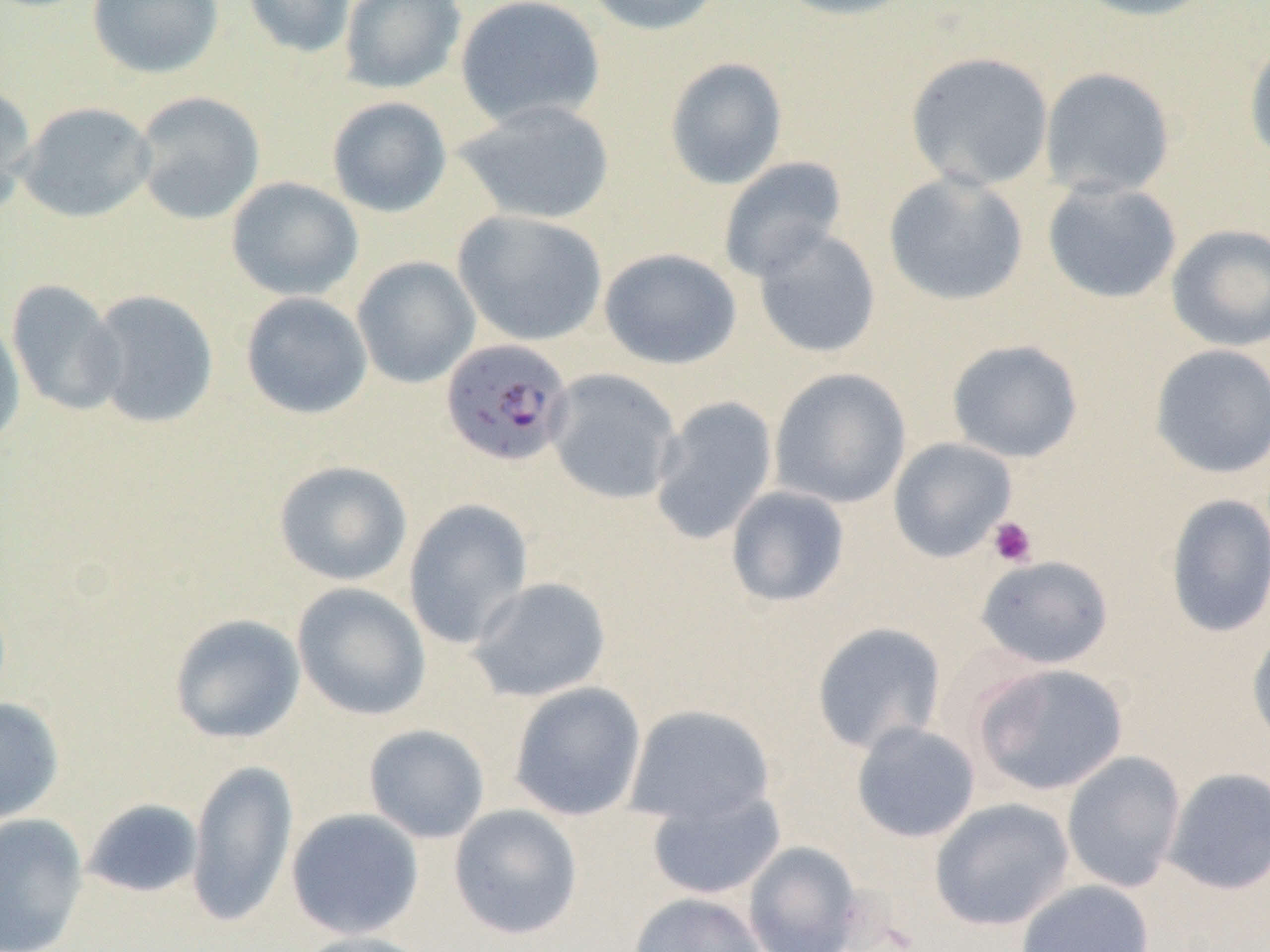

Summary:
  - Coordinate format: approximate bounding boxes as named x1/y1/x2/y2 corners in pixels
  - Uninfected red blood cell locations: (x1=86, y1=0, x2=224, y2=79), (x1=243, y1=0, x2=357, y2=59), (x1=338, y1=0, x2=467, y2=94), (x1=454, y1=0, x2=605, y2=129), (x1=582, y1=0, x2=729, y2=36), (x1=771, y1=0, x2=920, y2=21), (x1=1070, y1=0, x2=1220, y2=22), (x1=1244, y1=35, x2=1270, y2=167), (x1=904, y1=51, x2=1055, y2=192), (x1=664, y1=57, x2=788, y2=190), (x1=1039, y1=67, x2=1176, y2=199), (x1=0, y1=81, x2=37, y2=216), (x1=132, y1=91, x2=266, y2=225), (x1=327, y1=96, x2=452, y2=217), (x1=453, y1=99, x2=616, y2=225), (x1=17, y1=102, x2=156, y2=223), (x1=718, y1=157, x2=848, y2=283), (x1=883, y1=171, x2=1029, y2=306), (x1=225, y1=176, x2=363, y2=302), (x1=1042, y1=179, x2=1182, y2=304), (x1=452, y1=210, x2=607, y2=346), (x1=1165, y1=223, x2=1270, y2=352), (x1=752, y1=227, x2=882, y2=359), (x1=598, y1=247, x2=741, y2=370), (x1=351, y1=256, x2=481, y2=388), (x1=6, y1=278, x2=124, y2=416), (x1=85, y1=289, x2=219, y2=429), (x1=240, y1=291, x2=373, y2=419), (x1=0, y1=313, x2=26, y2=452), (x1=946, y1=339, x2=1084, y2=463), (x1=1150, y1=343, x2=1270, y2=479), (x1=768, y1=367, x2=912, y2=510), (x1=546, y1=368, x2=682, y2=505), (x1=649, y1=396, x2=778, y2=545), (x1=888, y1=437, x2=1017, y2=562), (x1=273, y1=459, x2=413, y2=586), (x1=725, y1=486, x2=850, y2=607), (x1=1165, y1=493, x2=1270, y2=638), (x1=403, y1=498, x2=534, y2=650), (x1=975, y1=554, x2=1114, y2=670), (x1=468, y1=576, x2=612, y2=702), (x1=291, y1=582, x2=431, y2=721), (x1=169, y1=613, x2=305, y2=744), (x1=811, y1=622, x2=947, y2=755), (x1=1247, y1=625, x2=1270, y2=753), (x1=972, y1=662, x2=1128, y2=796), (x1=509, y1=682, x2=646, y2=821), (x1=0, y1=697, x2=65, y2=823), (x1=624, y1=704, x2=775, y2=825), (x1=851, y1=721, x2=981, y2=843), (x1=363, y1=724, x2=490, y2=843), (x1=1061, y1=751, x2=1186, y2=893), (x1=186, y1=758, x2=298, y2=928), (x1=1163, y1=767, x2=1270, y2=895), (x1=646, y1=788, x2=786, y2=901), (x1=83, y1=798, x2=204, y2=898), (x1=930, y1=798, x2=1075, y2=931), (x1=448, y1=803, x2=583, y2=939), (x1=286, y1=808, x2=425, y2=940), (x1=0, y1=812, x2=89, y2=952), (x1=742, y1=841, x2=864, y2=952), (x1=1015, y1=879, x2=1155, y2=952), (x1=628, y1=892, x2=767, y2=952), (x1=289, y1=930, x2=436, y2=952)
  - Plasmodium falciparum-infected red blood cell locations: (x1=440, y1=338, x2=574, y2=467)
  - Platelet locations: (x1=987, y1=516, x2=1037, y2=567)
  - Slide-level diagnosis: Plasmodium falciparum
  - Field of view: single
  - Magnification: 1000x
  - Preparation: thin blood smear
  - Image size: 1270×952 pixels
  - Modality: optical microscopy